Assess this cell for malaria.
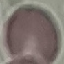

It is uninfected.

preparation: thin blood film
image_type: cell patch, automatically extracted from a larger field of view and resized to 64 × 64 pixels
stain: Giemsa
capture: smartphone through the microscope eyepiece